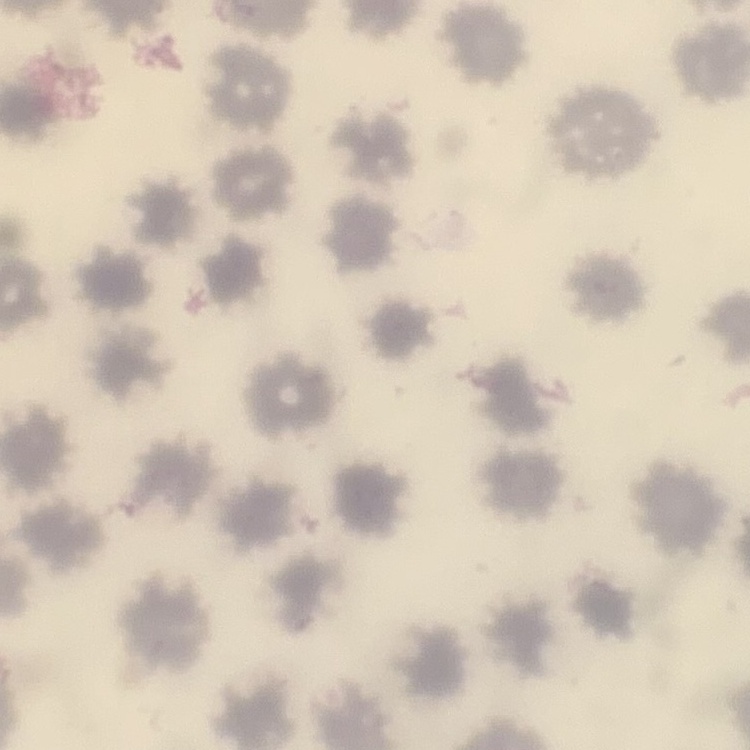

erythrocyte morphology = no rouleaux formation
stain = Field's or Giemsa
preparation = thin peripheral smear
image type = square crop of a larger photomicrograph